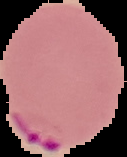

image size = 127×157 pixels
image type = cell region segmented out of the field of view; surrounding area masked to black
result = Plasmodium parasites identified
preparation = thin blood smear